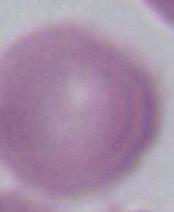
magnification = 1000x
identification = erythrocyte
modality = micrograph